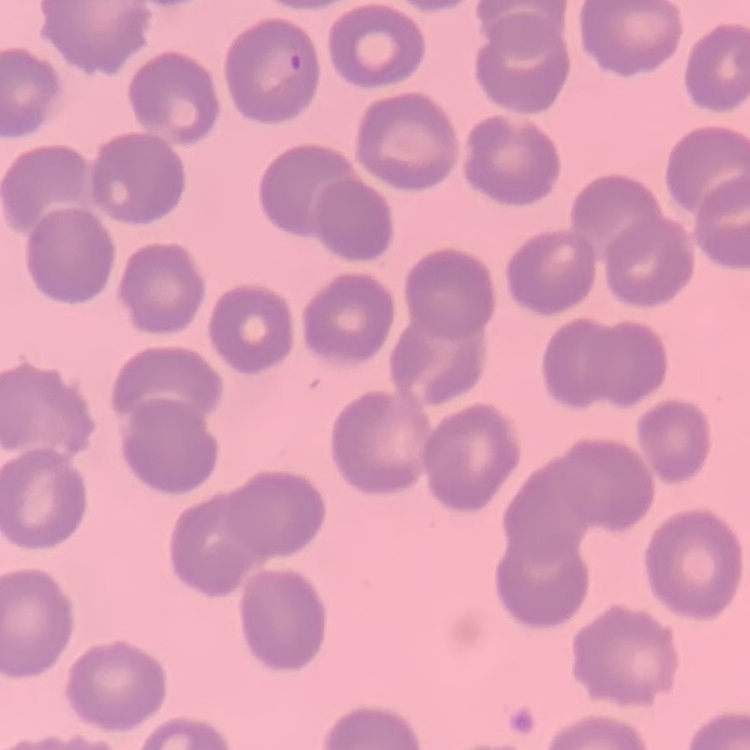
Summary:
  - Red blood cell morphology: no rouleaux formation
  - Preparation: thin peripheral smear
  - Image type: square crop of a larger photomicrograph
  - Stain: Field's or Giemsa